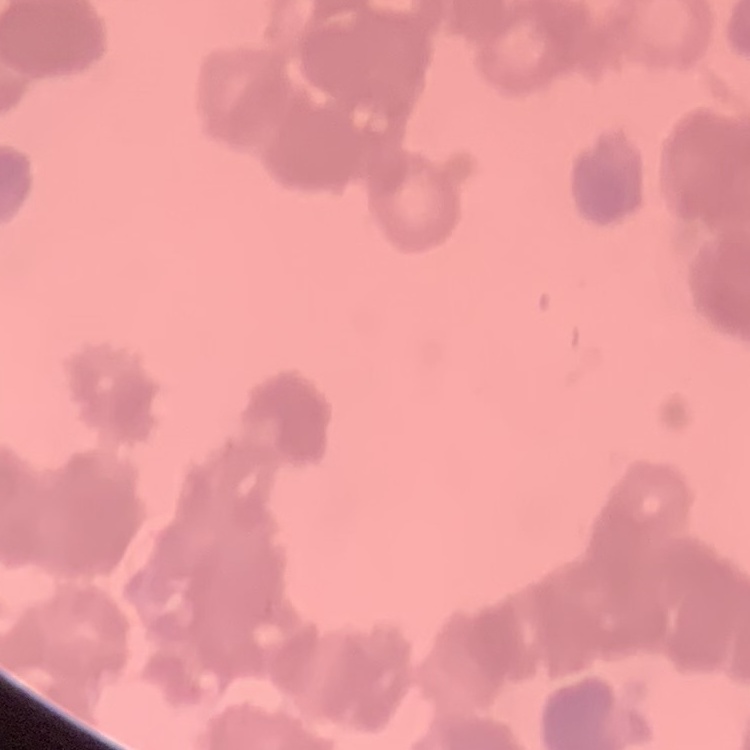
The erythrocytes exhibit rouleaux formation. Field's or Giemsa stain. One tile cut from a larger photomicrograph. Thin blood smear.